Comment on the morphology of the red blood cells.
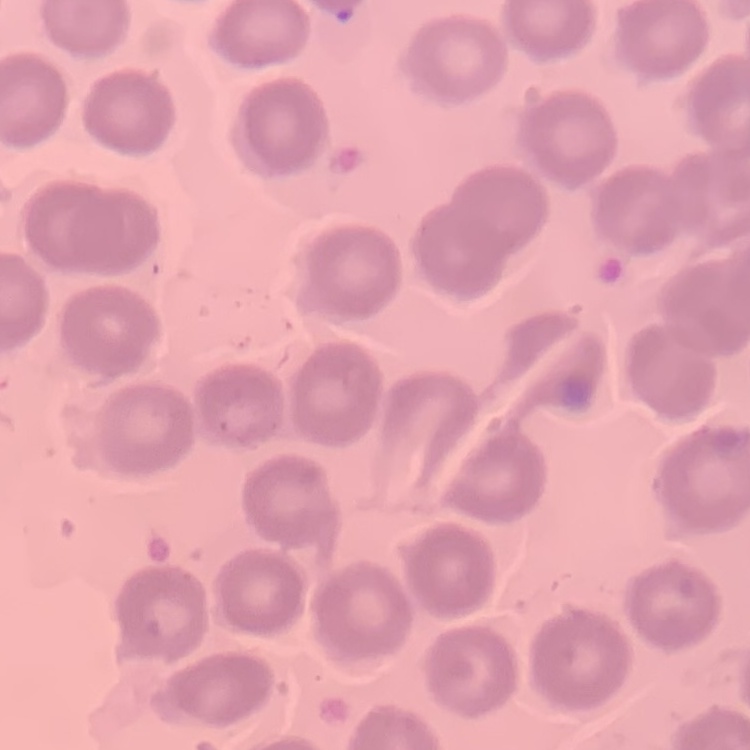
They show no rouleaux formation.

{
  "preparation": "thin blood smear",
  "image_type": "one tile cut from a larger photomicrograph",
  "stain": "Field's or Giemsa"
}